Give the extent of all uninfected red blood cells.
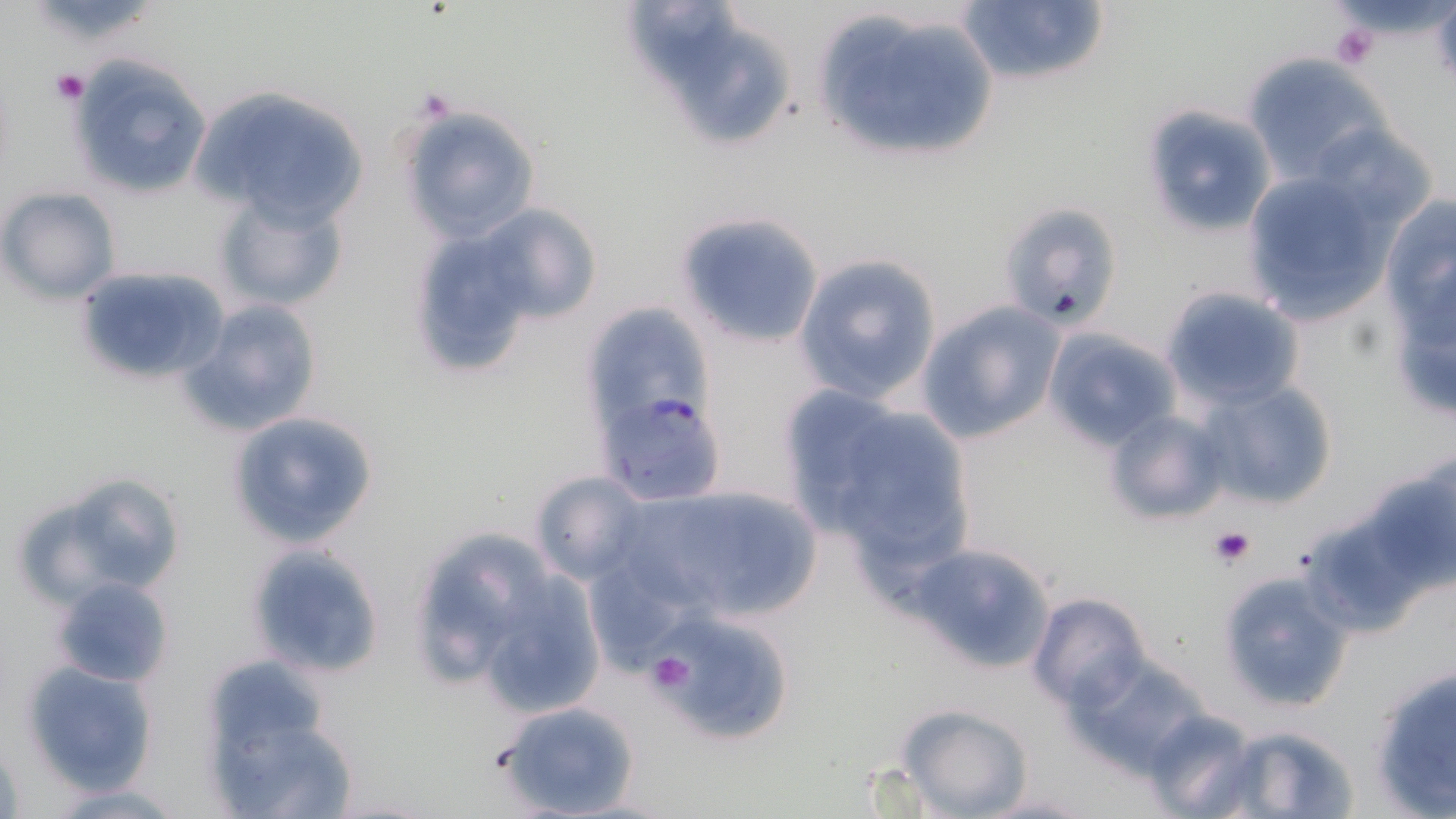

Approximate bounding boxes as [x1, y1, x2, y2] in pixels.
Uninfected red blood cells: [627, 0, 743, 83], [954, 0, 1111, 90], [809, 7, 1002, 167], [685, 31, 792, 143], [1242, 53, 1394, 187], [69, 57, 213, 200], [187, 85, 375, 231], [1138, 105, 1276, 237], [398, 106, 539, 243], [1236, 165, 1409, 323], [0, 187, 119, 303], [212, 188, 350, 314], [474, 202, 603, 328], [998, 202, 1123, 332], [673, 211, 825, 348], [1380, 223, 1456, 424], [430, 242, 528, 347], [792, 253, 942, 406], [74, 264, 232, 385], [1160, 287, 1304, 409], [178, 299, 322, 438], [915, 301, 1064, 445], [589, 304, 709, 410], [1043, 329, 1179, 451], [1193, 376, 1340, 511], [775, 385, 915, 526], [798, 399, 980, 580], [1102, 409, 1227, 526], [225, 410, 382, 550], [1365, 456, 1456, 595], [35, 470, 187, 602], [527, 470, 649, 585], [613, 484, 823, 626], [402, 524, 558, 690], [244, 542, 385, 681], [910, 542, 1059, 672], [474, 571, 606, 717], [1217, 572, 1352, 711], [1027, 592, 1153, 713], [647, 608, 793, 746], [1064, 652, 1216, 775], [1367, 660, 1456, 818], [22, 661, 160, 794], [496, 699, 643, 819], [896, 704, 1034, 818], [207, 707, 355, 819], [1141, 708, 1260, 818], [1219, 726, 1360, 819], [43, 781, 194, 816], [980, 791, 1093, 817].

Summary:
  - Plasmodium falciparum-infected red blood cell locations: [599, 390, 727, 506]
  - Platelet locations: [1429, 2, 1456, 87], [1331, 23, 1380, 69], [49, 67, 89, 105], [1208, 525, 1256, 569], [644, 652, 696, 696]
  - Slide-level diagnosis: Plasmodium falciparum
  - Stain: May-Grünwald-Giemsa
  - Magnification: 1000x
  - Modality: light microscopy
  - Field of view: one of a larger specimen
  - Image size: 1456×819 pixels
  - Preparation: thin blood smear